Classify this cell by malaria status.
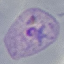
It is parasitized.

Thin smear of blood. Photographed with a smartphone camera at the microscope eyepiece. Giemsa-stained preparation. Automatically extracted cell patch, resized to 64 × 64 pixels.